Assess this cell for malaria.
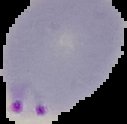

Parasitized.

The area outside the segmented cell region is set to black. Image is 127×124 pixels. From a thin blood smear.